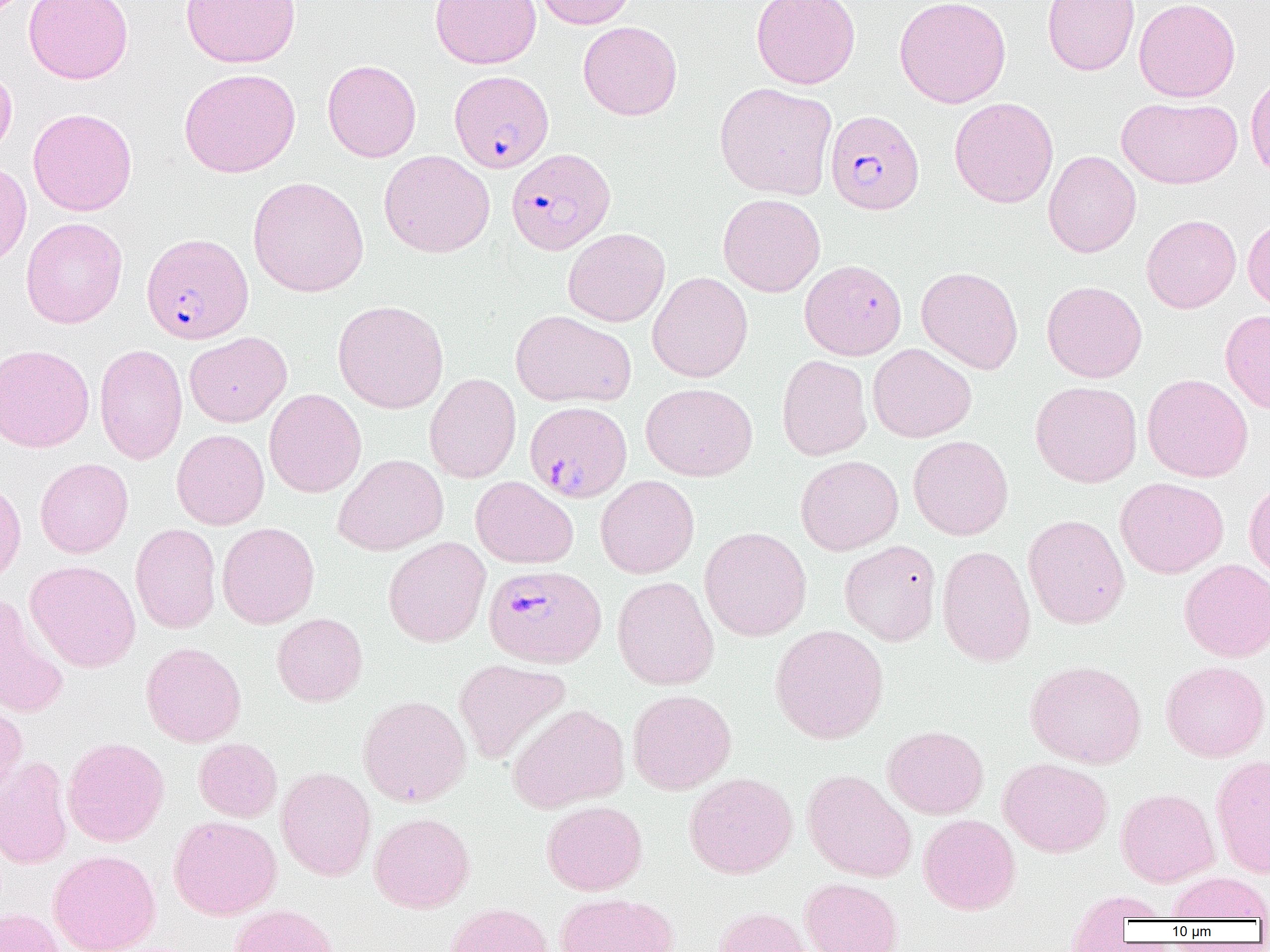

slide-level diagnosis = Plasmodium falciparum
magnification = 1000x
preparation = thin blood film
uninfected red blood cell locations (subset) = approximate bounding boxes as named x1/y1/x2/y2 corners in pixels: (x1=23, y1=0, x2=133, y2=84), (x1=180, y1=0, x2=301, y2=68), (x1=430, y1=0, x2=542, y2=69), (x1=534, y1=0, x2=636, y2=29), (x1=751, y1=0, x2=860, y2=89), (x1=894, y1=0, x2=1011, y2=108), (x1=1042, y1=0, x2=1140, y2=76), (x1=1134, y1=0, x2=1240, y2=102), (x1=578, y1=21, x2=682, y2=121), (x1=322, y1=59, x2=421, y2=162), (x1=0, y1=65, x2=17, y2=159), (x1=179, y1=68, x2=300, y2=178), (x1=1245, y1=71, x2=1270, y2=181), (x1=715, y1=82, x2=837, y2=200), (x1=949, y1=97, x2=1059, y2=208), (x1=1117, y1=97, x2=1242, y2=189), (x1=28, y1=108, x2=137, y2=216), (x1=379, y1=150, x2=495, y2=257), (x1=1043, y1=150, x2=1141, y2=257), (x1=0, y1=162, x2=32, y2=268), (x1=248, y1=176, x2=369, y2=298), (x1=718, y1=193, x2=825, y2=297), (x1=1141, y1=214, x2=1241, y2=313), (x1=1243, y1=216, x2=1270, y2=312), (x1=20, y1=217, x2=127, y2=328), (x1=563, y1=227, x2=670, y2=327), (x1=916, y1=266, x2=1023, y2=374), (x1=647, y1=271, x2=753, y2=382), (x1=1042, y1=281, x2=1147, y2=383), (x1=332, y1=300, x2=449, y2=414), (x1=1220, y1=309, x2=1270, y2=413), (x1=511, y1=310, x2=636, y2=408), (x1=184, y1=332, x2=292, y2=428), (x1=867, y1=343, x2=977, y2=443), (x1=0, y1=344, x2=94, y2=452), (x1=94, y1=344, x2=187, y2=465), (x1=776, y1=355, x2=872, y2=460), (x1=424, y1=373, x2=521, y2=483), (x1=1142, y1=373, x2=1253, y2=482), (x1=1029, y1=381, x2=1142, y2=488), (x1=641, y1=382, x2=757, y2=481), (x1=264, y1=388, x2=367, y2=498), (x1=171, y1=429, x2=269, y2=530), (x1=908, y1=435, x2=1013, y2=540), (x1=334, y1=454, x2=448, y2=555), (x1=795, y1=455, x2=903, y2=555), (x1=35, y1=458, x2=133, y2=558), (x1=471, y1=475, x2=578, y2=569), (x1=595, y1=475, x2=699, y2=578), (x1=0, y1=476, x2=26, y2=587), (x1=1115, y1=477, x2=1229, y2=578), (x1=1243, y1=478, x2=1270, y2=582), (x1=1023, y1=514, x2=1130, y2=629), (x1=216, y1=522, x2=319, y2=629), (x1=130, y1=523, x2=222, y2=633), (x1=700, y1=526, x2=811, y2=641), (x1=383, y1=537, x2=491, y2=647), (x1=839, y1=540, x2=942, y2=646), (x1=937, y1=544, x2=1036, y2=667), (x1=1179, y1=558, x2=1270, y2=662), (x1=25, y1=560, x2=140, y2=672), (x1=612, y1=576, x2=719, y2=690), (x1=0, y1=594, x2=69, y2=719), (x1=272, y1=613, x2=368, y2=706), (x1=769, y1=624, x2=889, y2=744), (x1=141, y1=642, x2=246, y2=747), (x1=453, y1=658, x2=571, y2=765), (x1=1025, y1=660, x2=1146, y2=768), (x1=1160, y1=660, x2=1270, y2=762), (x1=627, y1=689, x2=736, y2=794), (x1=358, y1=694, x2=471, y2=807), (x1=0, y1=698, x2=28, y2=803), (x1=507, y1=703, x2=629, y2=812), (x1=882, y1=725, x2=988, y2=819), (x1=62, y1=737, x2=169, y2=847), (x1=193, y1=738, x2=282, y2=822), (x1=1211, y1=753, x2=1270, y2=878), (x1=0, y1=756, x2=74, y2=870), (x1=998, y1=758, x2=1112, y2=857), (x1=276, y1=766, x2=376, y2=881), (x1=802, y1=769, x2=917, y2=882), (x1=684, y1=772, x2=798, y2=878), (x1=1115, y1=788, x2=1219, y2=887), (x1=542, y1=800, x2=647, y2=895), (x1=369, y1=812, x2=475, y2=913), (x1=918, y1=813, x2=1021, y2=915), (x1=169, y1=815, x2=281, y2=920), (x1=48, y1=850, x2=161, y2=952), (x1=1166, y1=872, x2=1270, y2=921), (x1=799, y1=878, x2=902, y2=952), (x1=1064, y1=889, x2=1172, y2=942), (x1=555, y1=892, x2=678, y2=952), (x1=444, y1=902, x2=554, y2=952), (x1=228, y1=904, x2=339, y2=952), (x1=712, y1=906, x2=820, y2=952), (x1=0, y1=907, x2=67, y2=952)
field of view = single
modality = light microscopy
image size = 1270×952 pixels
Plasmodium falciparum-infected red blood cell locations (subset) = approximate bounding boxes as named x1/y1/x2/y2 corners in pixels: (x1=449, y1=70, x2=553, y2=173), (x1=826, y1=109, x2=924, y2=214), (x1=506, y1=148, x2=615, y2=255), (x1=142, y1=233, x2=253, y2=344), (x1=524, y1=401, x2=632, y2=502)